Report the malaria status of this cell.
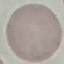

Uninfected.

image type = automatically extracted cell patch, resized to 64 × 64 pixels
capture = smartphone camera at the microscope eyepiece
preparation = thin blood smear
stain = Giemsa